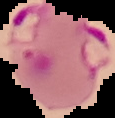 Cell region segmented out of the field of view; the surrounding area is masked to black. From a thin blood smear. Image is 115×118 pixels. Malaria status: parasitized.